Report the malaria status of this cell.
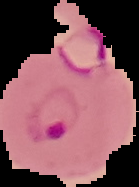
It is parasitized.

Image is 139×187 pixels. From a thin blood smear. Cell region segmented out of the field of view; the surrounding area is masked to black.